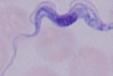

Summary:
  - Magnification: 1000x
  - Identification: trypanosome
  - Modality: photomicrograph